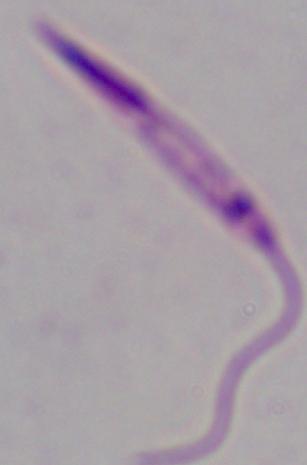
identification = Leishmania
modality = micrograph
magnification = 1000x